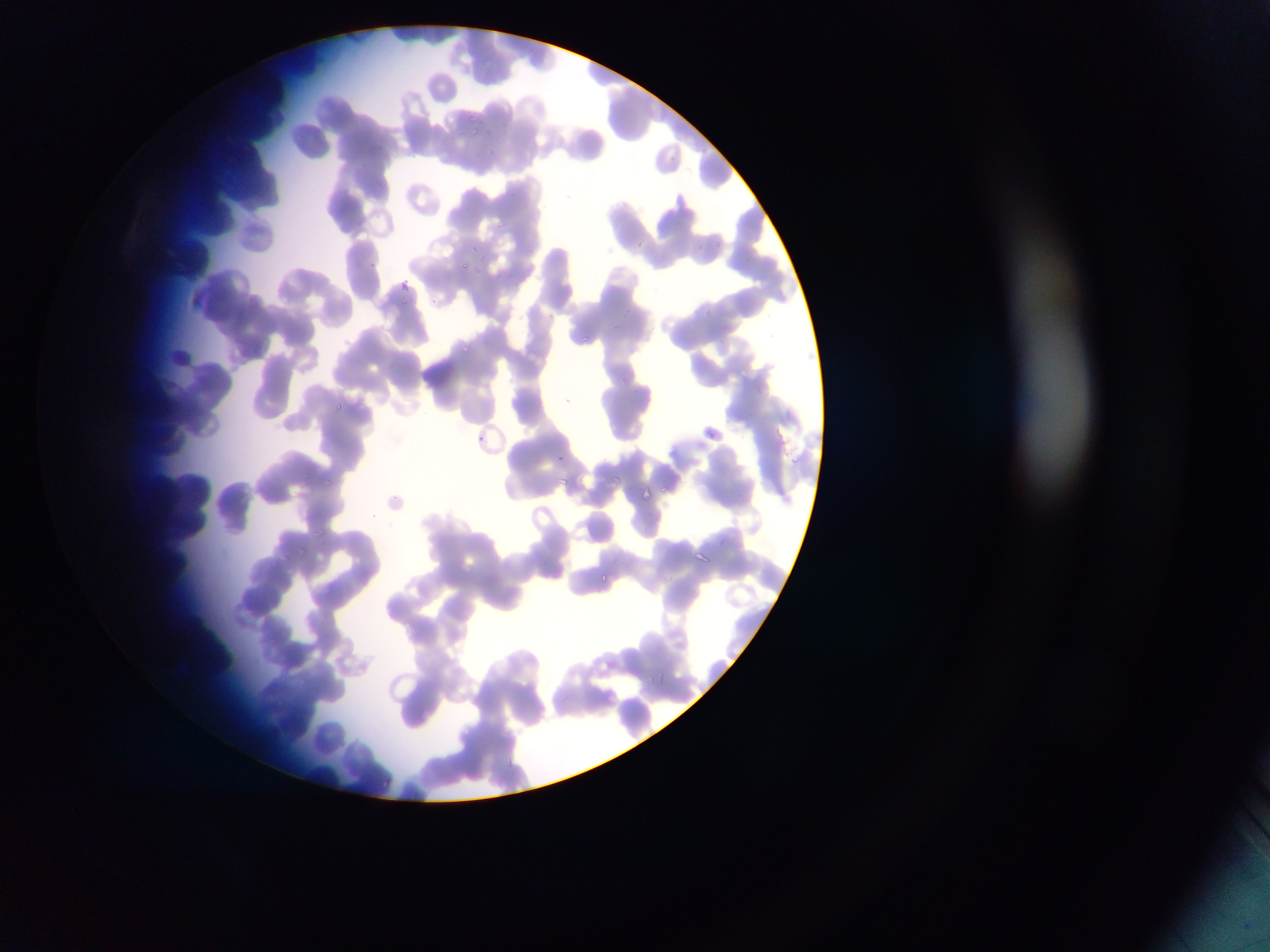
Approximate bounding boxes as left top right bottom in pixels. Plasmodium parasite locations: 467 113 483 128; 470 125 484 139; 489 147 497 159; 712 239 723 253; 697 242 707 253; 468 243 481 254; 476 255 491 265; 460 260 474 272; 369 261 379 273; 470 268 482 277; 494 271 504 284; 395 275 412 290; 398 294 413 305; 702 307 714 318; 579 333 593 348; 457 341 474 353; 622 376 634 389; 332 400 343 414; 706 427 717 441; 474 431 486 446; 554 452 569 465; 303 472 311 480; 613 475 624 483; 557 476 571 486; 322 478 332 488; 660 483 672 495; 641 487 653 501; 314 529 325 538; 295 544 306 555; 600 572 614 587; 655 672 668 683; 277 697 289 708; 380 778 391 790. Collected in Ghana. One field of view. Image is 1270×952 pixels. Thin blood film. Photographed through a microscope with a mobile-phone camera.